Assess the morphology of the erythrocytes.
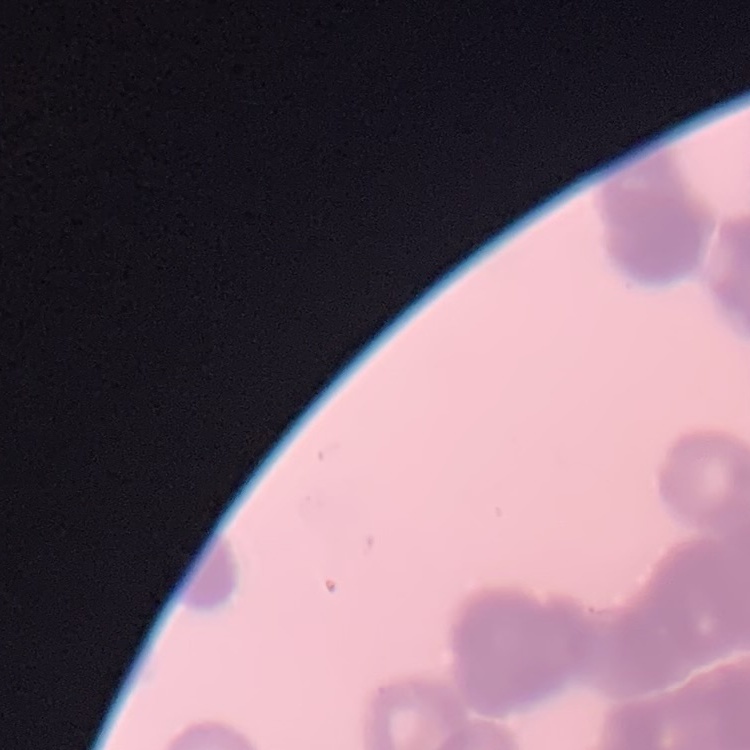
Rouleaux formation.

{
  "image_type": "square crop of a larger photomicrograph",
  "stain": "Field's or Giemsa",
  "preparation": "thin blood film"
}